Give the extent of all uninfected red blood cells.
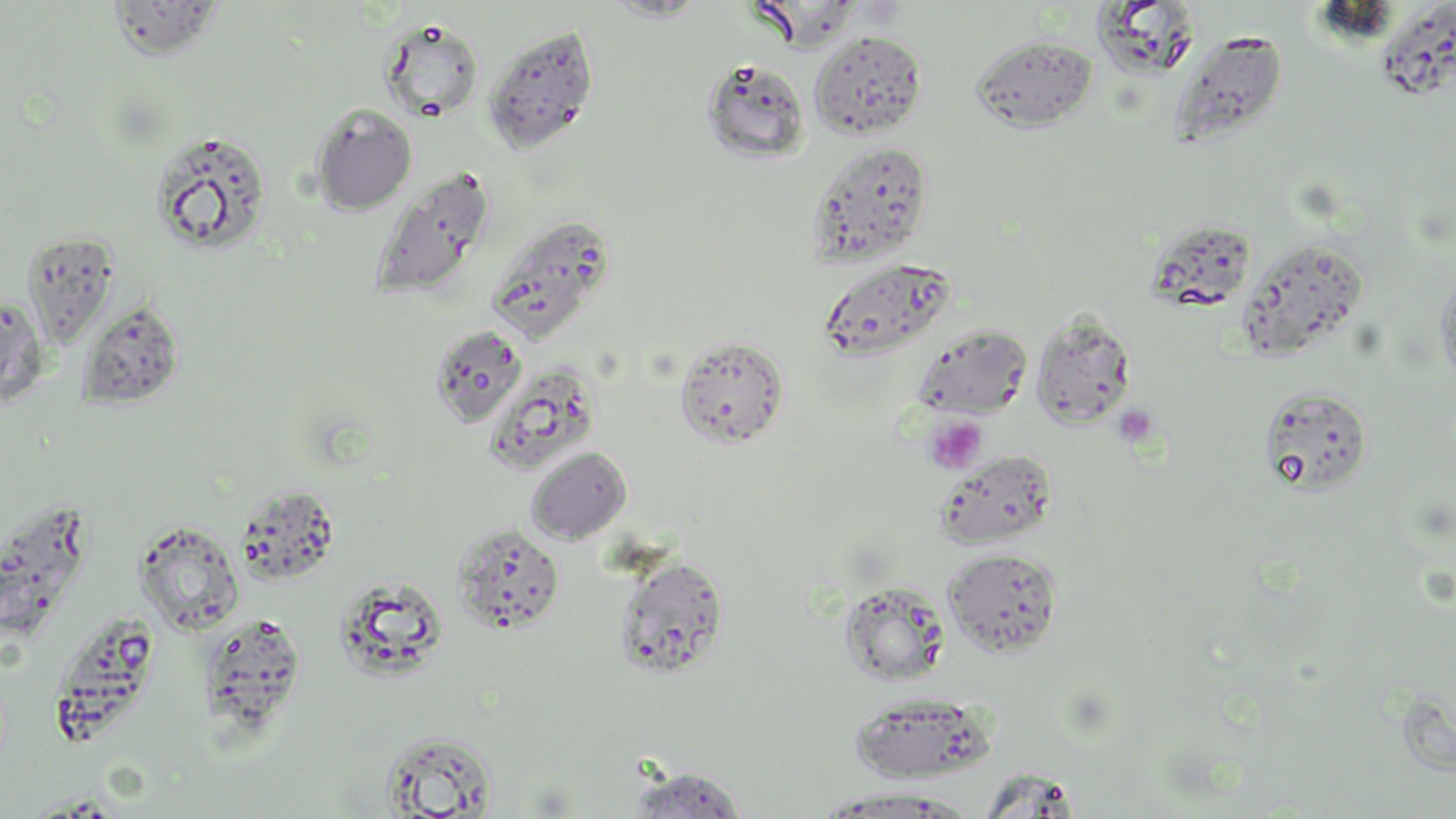

Approximate bounding boxes as (x1, y1, x2, y2) in pixels.
Uninfected red blood cells: (105, 0, 228, 60), (602, 0, 713, 22), (751, 0, 860, 51), (1090, 3, 1203, 79), (379, 18, 486, 122), (482, 23, 600, 154), (809, 30, 927, 141), (1168, 30, 1288, 150), (968, 34, 1098, 132), (701, 58, 811, 164), (309, 104, 417, 215), (149, 129, 273, 255), (808, 142, 934, 265), (370, 168, 495, 300), (487, 213, 618, 340), (22, 232, 118, 349), (1236, 238, 1369, 360), (819, 258, 956, 360), (1434, 267, 1456, 398), (0, 294, 50, 409), (76, 300, 185, 410), (1030, 308, 1136, 430), (428, 324, 527, 427), (911, 324, 1033, 419), (674, 334, 789, 448), (484, 363, 600, 475), (1258, 386, 1374, 496), (526, 446, 632, 545), (934, 450, 1059, 550), (134, 520, 245, 635), (450, 522, 565, 634), (943, 547, 1063, 657), (613, 555, 730, 680), (839, 582, 951, 687), (198, 612, 307, 736), (847, 692, 993, 783), (379, 729, 499, 817), (624, 765, 749, 819), (816, 789, 975, 817).

Platelet locations: (1111, 403, 1160, 448), (924, 414, 987, 475). Slide-level diagnosis: negative for blood parasites. Image is 1456×819 pixels. One field of a larger specimen. Optical microscopy. 1000x magnification. May-Grünwald-Giemsa-stained preparation. Thin blood smear.